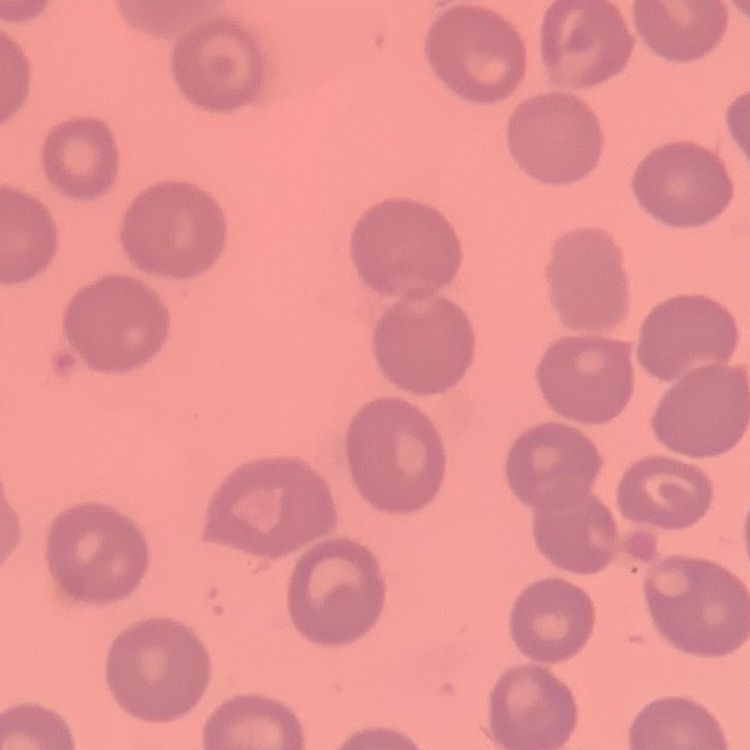
{
  "erythrocyte_morphology": "no rouleaux formation",
  "preparation": "thin peripheral smear",
  "stain": "Field's or Giemsa",
  "image_type": "one tile cut from a larger photomicrograph"
}